Name the parasite shown.
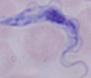
A trypanosome.

1000x magnification. Micrograph.